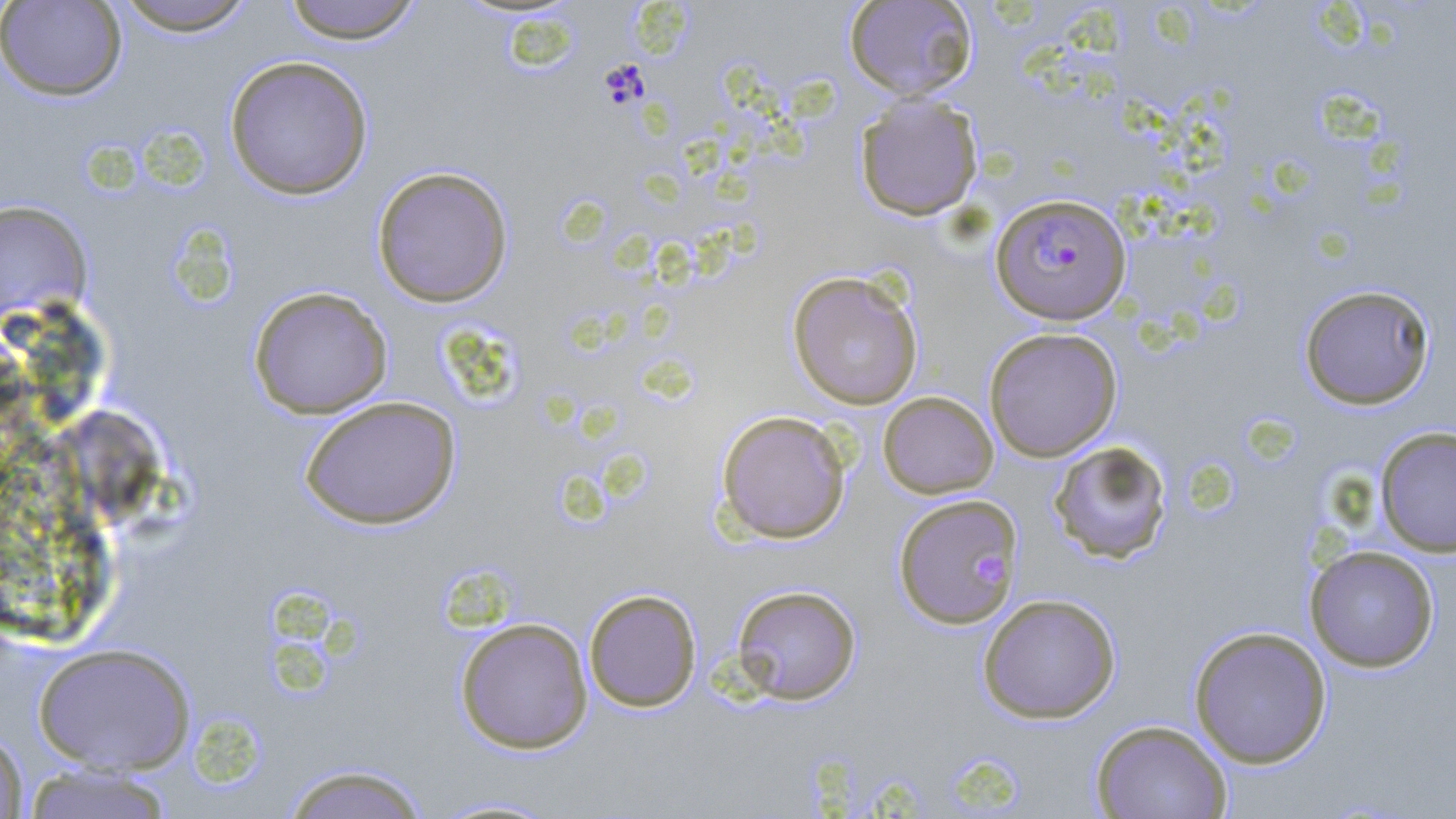
Summary:
  - Coordinate format: approximate bounding boxes as (x1,y1)-(x2,y2) corner pairs in pixels
  - Uninfected red blood cell locations: (1,0)-(127,101), (109,0)-(261,36), (279,0)-(425,44), (843,1)-(978,100), (224,55)-(374,200), (854,93)-(984,221), (371,166)-(514,308), (0,200)-(93,321), (787,270)-(923,410), (1298,284)-(1437,410), (248,286)-(393,419), (983,327)-(1122,462), (878,391)-(998,499), (299,395)-(462,530), (55,405)-(170,526), (715,409)-(851,544), (1374,426)-(1456,557), (1049,440)-(1173,564), (893,493)-(1023,629), (1304,544)-(1440,673), (731,584)-(862,705), (583,588)-(702,712), (978,593)-(1122,724), (455,617)-(593,754), (1188,625)-(1333,768), (33,643)-(196,775), (1091,719)-(1232,819), (0,728)-(28,818), (277,763)-(434,819), (17,764)-(179,818), (426,795)-(566,817)
  - Platelet locations: (974,549)-(1010,587)
  - Plasmodium falciparum-infected red blood cell locations: (991,193)-(1132,325)
  - Slide-level diagnosis: Plasmodium falciparum
  - Image size: 1456×819 pixels
  - Stain: May-Grünwald-Giemsa
  - Field of view: single
  - Magnification: 1000x
  - Modality: light microscopy
  - Preparation: thin blood smear